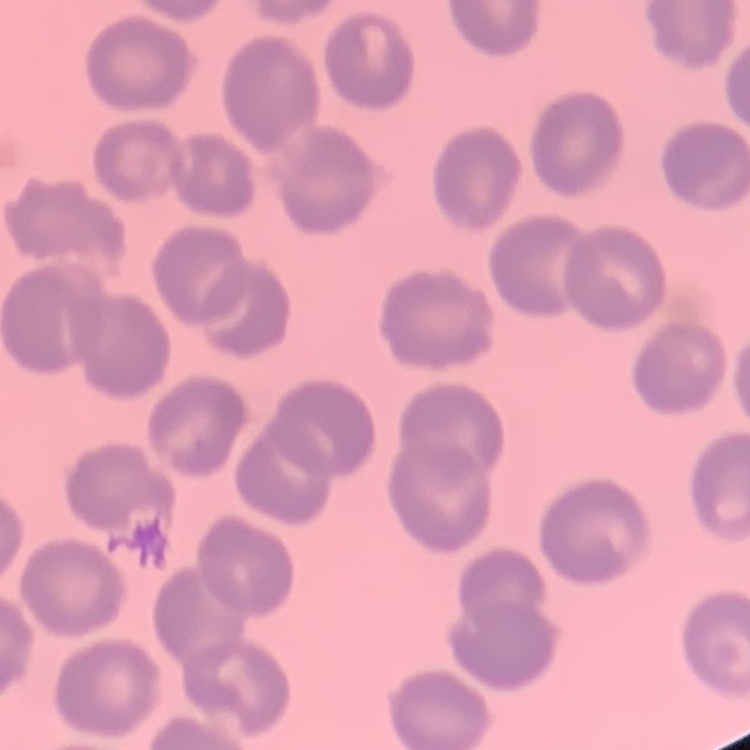

The erythrocytes exhibit no rouleaux formation. Field's or Giemsa stain. Square crop of a larger photomicrograph. Thin peripheral smear.